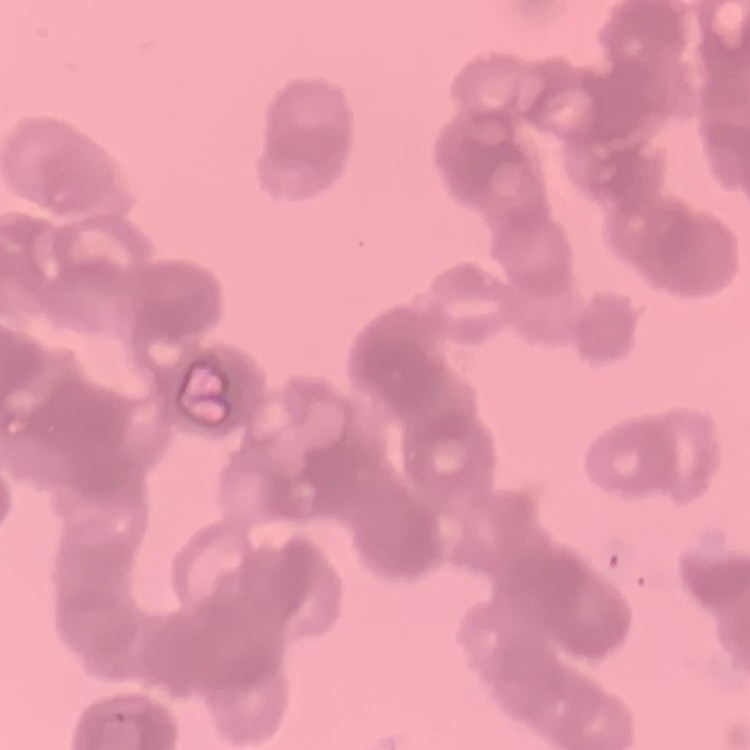

Summary:
  - Red blood cell morphology: rouleaux formation
  - Stain: Field's or Giemsa
  - Image type: square crop of a larger photomicrograph
  - Preparation: thin blood smear